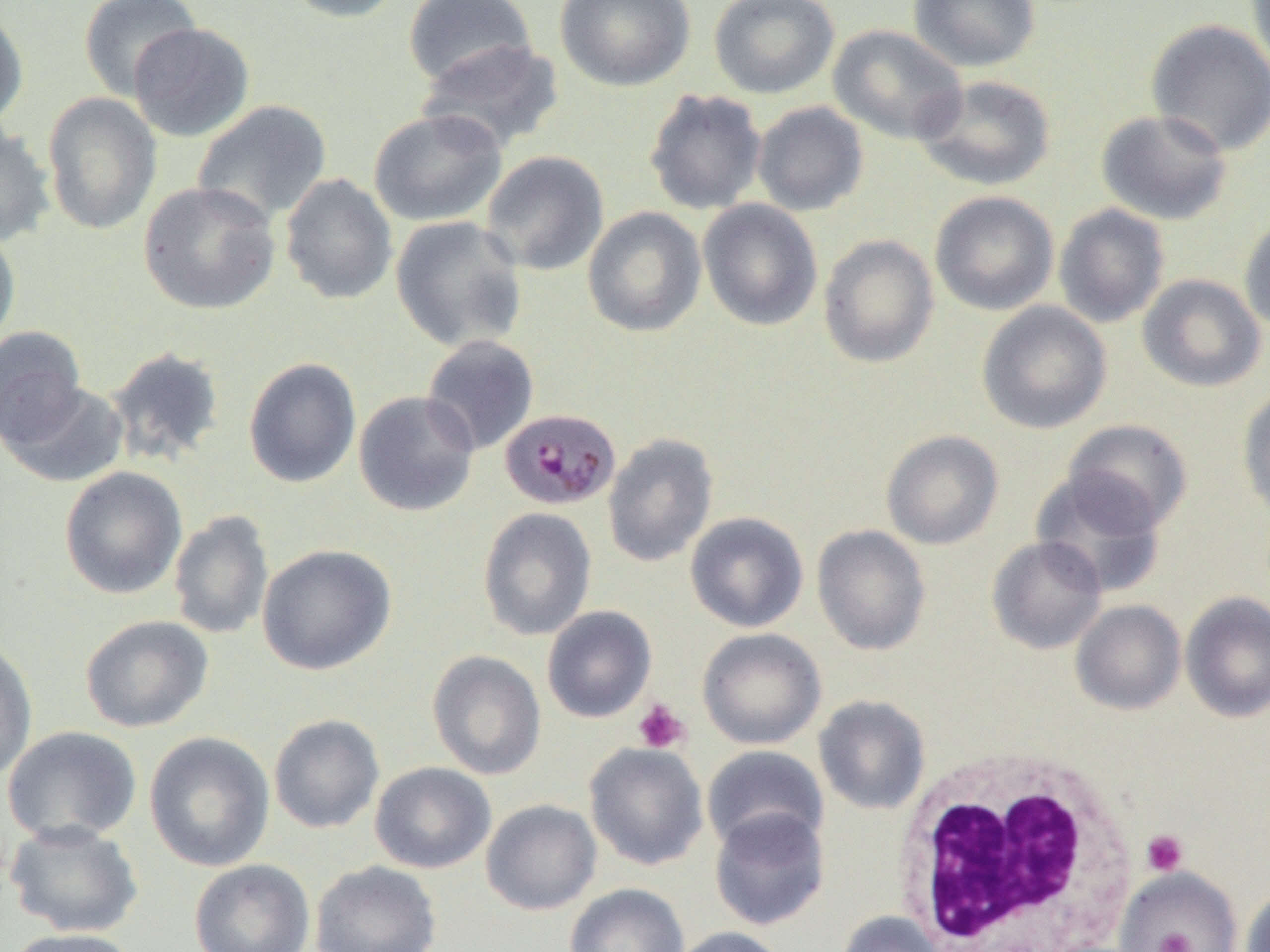
Summary:
  - Coordinate format: approximate bounding boxes as (x1,y1)-(x2,y2) corner pairs in pixels
  - Uninfected red blood cell locations: (79,0)-(201,100), (281,0)-(408,23), (554,0)-(696,91), (708,0)-(840,99), (907,0)-(1041,72), (1245,0)-(1270,83), (403,1)-(538,90), (0,6)-(29,130), (1145,19)-(1270,157), (127,22)-(255,142), (827,23)-(968,146), (416,38)-(565,152), (914,75)-(1057,190), (643,88)-(767,216), (42,91)-(162,235), (191,99)-(333,225), (752,101)-(869,217), (367,109)-(507,226), (1096,109)-(1233,225), (0,125)-(56,247), (480,150)-(609,276), (280,173)-(398,305), (138,181)-(281,316), (929,191)-(1059,316), (697,199)-(824,331), (1054,203)-(1170,328), (582,207)-(707,338), (1238,214)-(1270,334), (390,215)-(528,353), (0,225)-(21,353), (818,234)-(939,368), (1137,274)-(1266,393), (977,301)-(1112,434), (0,325)-(88,448), (421,335)-(540,455), (105,345)-(227,468), (243,357)-(361,489), (2,380)-(131,489), (1236,385)-(1270,520), (353,390)-(480,517), (1063,419)-(1192,534), (880,430)-(1004,550), (602,433)-(719,567), (59,466)-(188,600), (1030,470)-(1167,598), (478,507)-(597,641), (168,509)-(274,640), (685,511)-(809,632), (812,525)-(931,655), (986,535)-(1107,654), (257,543)-(397,675), (1180,591)-(1270,722), (1070,600)-(1186,715), (541,605)-(657,723), (80,614)-(214,732), (697,627)-(827,750), (0,638)-(38,783), (427,650)-(547,780), (813,695)-(931,815), (268,713)-(385,834), (2,725)-(142,845), (144,731)-(275,872), (584,742)-(709,870), (702,745)-(829,853), (370,762)-(496,873), (480,799)-(602,915), (709,807)-(830,931), (5,820)-(143,938), (189,859)-(315,952), (310,860)-(442,952), (1115,867)-(1243,951), (564,883)-(690,952), (1240,888)-(1270,952), (836,910)-(945,952), (669,926)-(790,952), (4,927)-(140,952)
  - Platelet locations: (633,700)-(690,753), (1141,830)-(1189,876), (1155,932)-(1194,952)
  - Plasmodium malariae-infected red blood cell locations: (499,407)-(624,512)
  - White blood cell locations: (893,749)-(1139,952)
  - Slide-level diagnosis: Plasmodium malariae
  - Magnification: 1000x
  - Image size: 1270×952 pixels
  - Modality: optical microscopy
  - Preparation: thin blood film
  - Field of view: one of a larger specimen